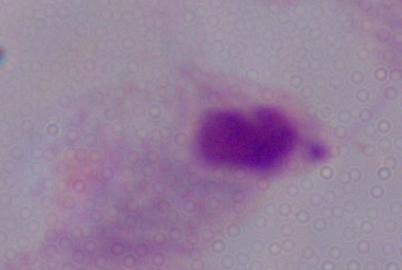
Summary:
  - Magnification: 1000x
  - Identification: trichomonad
  - Modality: photomicrograph